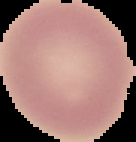

Image is 136×142 pixels. Segmented cell region on a black background. From a thin blood smear. Result: no Plasmodium parasites detected.